Locate every Plasmodium parasite.
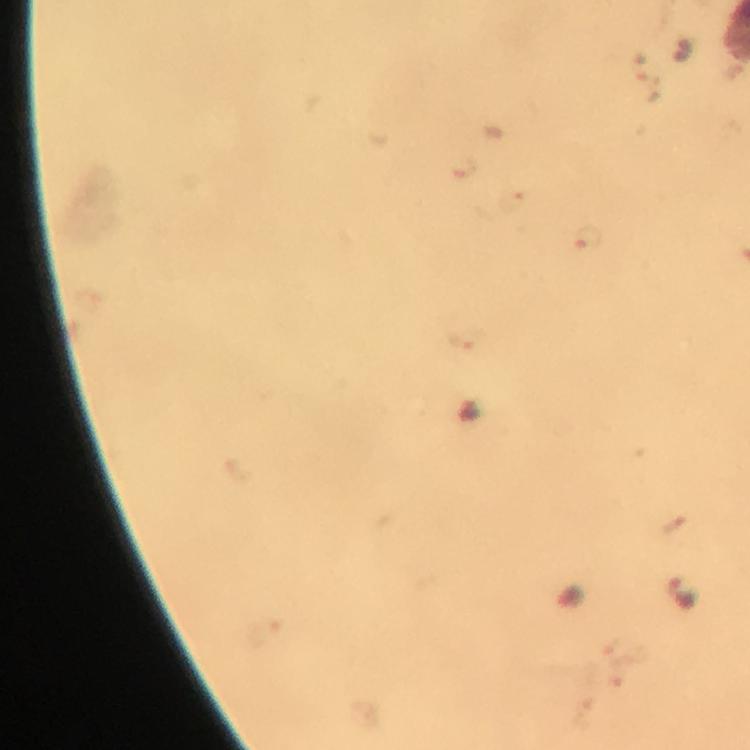

Approximate centers as [x, y] in pixels.
Plasmodium parasites: [680, 592].

Thick blood smear. 100x magnification. Giemsa stain. Immersion oil was used. Image is 750×750 pixels. Smartphone photograph taken through a microscope. A crop from one field of view. From a malaria diagnostic workup.